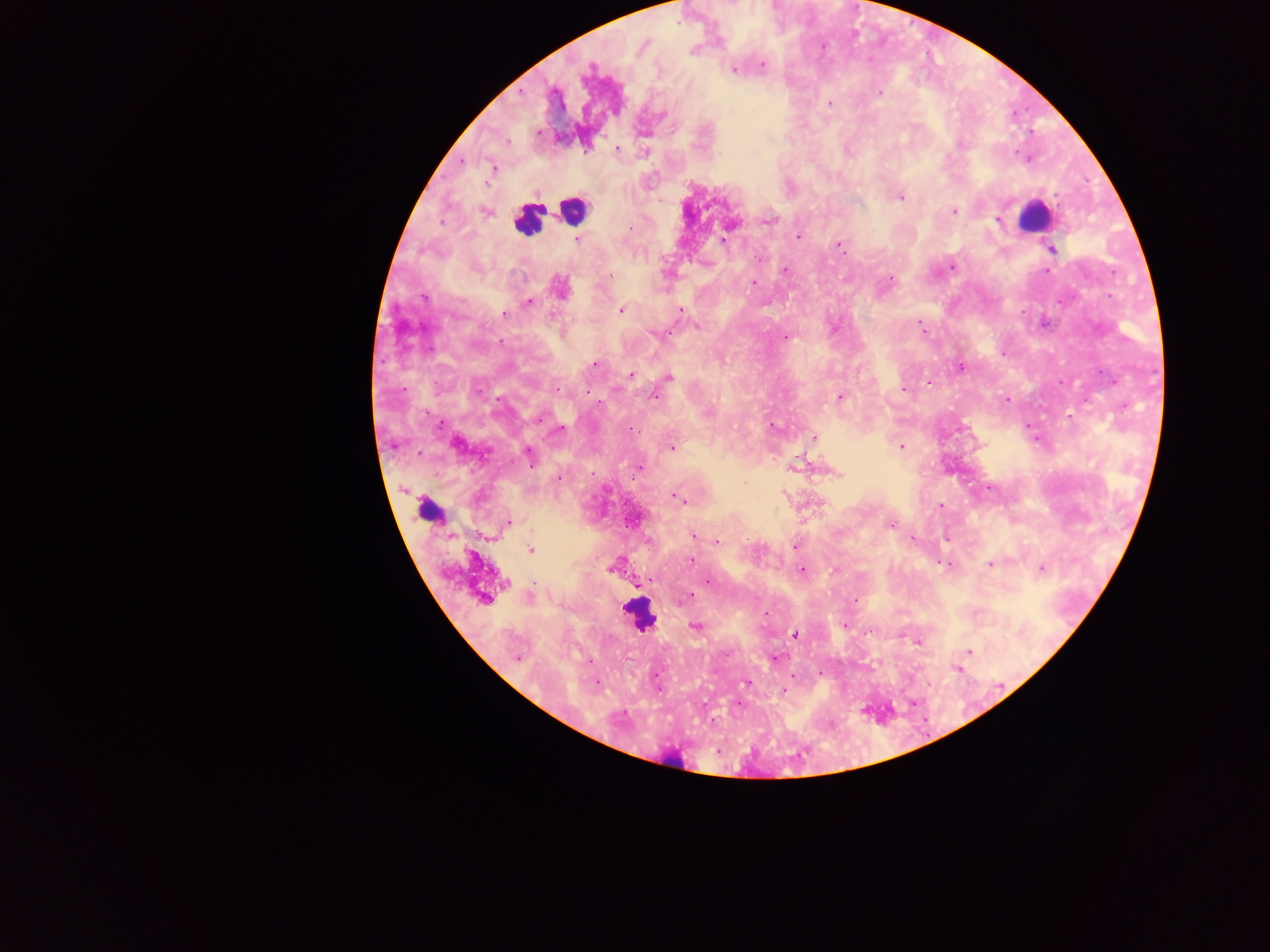
capture = mobile-phone photograph through a microscope
field of view = single
leukocyte locations = approximate centers as (x, y) in pixels: (572, 211), (1033, 216), (528, 220), (431, 511), (639, 615), (678, 763)
Plasmodium parasite locations = approximate centers as (x, y) in pixels: (763, 65), (590, 69), (733, 69), (879, 94), (829, 103), (538, 132), (617, 149), (493, 167), (901, 197), (954, 211), (484, 212), (997, 220), (770, 221), (631, 227), (798, 236), (724, 239), (577, 240), (840, 246), (1051, 250), (759, 259), (952, 267), (784, 269), (1046, 271), (609, 276), (891, 279), (754, 282), (560, 287), (424, 298), (528, 302), (621, 310), (681, 310), (504, 315), (697, 326), (921, 326), (659, 334), (785, 337), (595, 364), (960, 366), (631, 374), (669, 378), (928, 382), (904, 389), (558, 390), (655, 396), (840, 397), (1006, 399), (539, 419), (773, 427), (560, 429), (631, 429), (815, 438), (900, 446), (672, 447), (529, 455), (638, 468), (592, 473), (839, 474), (559, 477), (677, 498), (681, 500), (940, 505), (508, 523), (891, 525), (693, 536), (912, 539), (718, 541), (795, 546), (531, 549), (692, 561), (948, 564), (991, 564), (610, 568), (1042, 569), (801, 571), (651, 580), (707, 581), (506, 583), (530, 597), (690, 597), (485, 599), (855, 601), (695, 626), (794, 634), (918, 642), (968, 653), (517, 658), (775, 658), (957, 668), (597, 683), (746, 683), (783, 691)
preparation = thick blood smear
country = Ghana
image size = 1270×952 pixels